Classify this cell by malaria status.
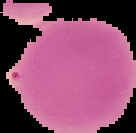

Uninfected.

Summary:
  - Image size: 136×133 pixels
  - Image type: segmented cell region with the area outside set to black
  - Preparation: thin blood film